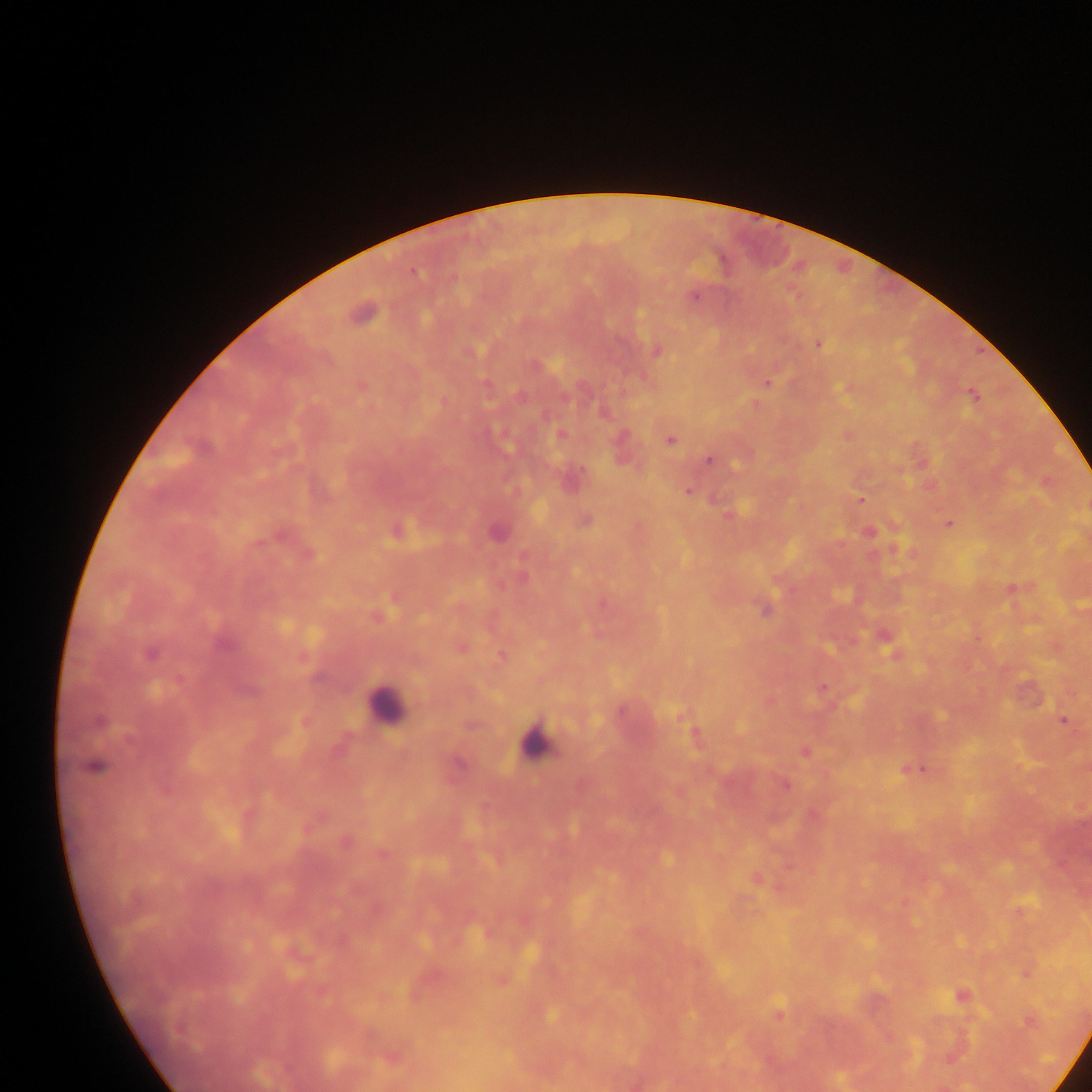 Approximate centers as x y in pixels. Plasmodium parasite locations: 413 272; 693 296; 362 313; 818 344; 657 352; 536 366; 487 383; 767 383; 361 387; 973 394; 519 396; 564 397; 603 413; 561 435; 623 436; 670 440; 709 460; 687 492; 861 499; 586 520; 949 525; 869 533; 1011 589; 764 609; 223 645; 461 647; 150 654; 501 655; 822 690; 620 711; 681 715; 1063 721; 99 722; 805 751; 458 764; 94 766; 915 770; 786 785; 343 842; 382 854; 961 996; 779 1011; 1029 1021. Leukocyte locations: 385 705; 538 740. Photographed through a microscope with a mobile-phone camera. Image is 1092×1092 pixels. Collected in Ghana. One field of view. Thick blood smear.